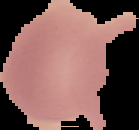
Summary:
  - Image size: 139×130 pixels
  - Malaria status: uninfected
  - Preparation: thin blood smear
  - Image type: segmented cell region on a black background